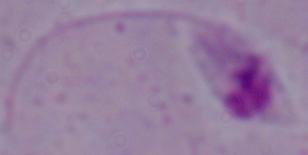
Captured at 1000x magnification. Photomicrograph. A Leishmania parasite is shown.